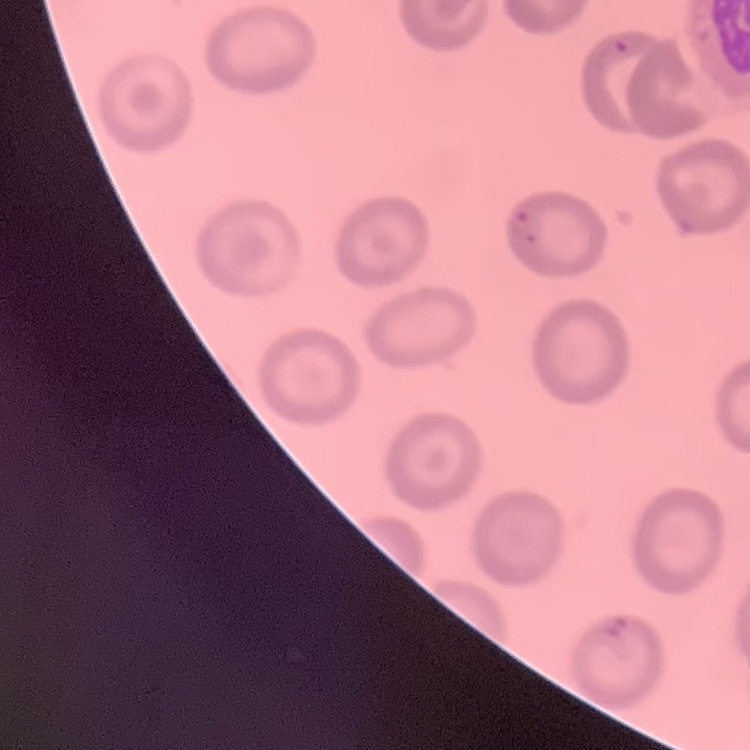
The red blood cells exhibit no rouleaux formation. Stained with either Field's or Giemsa. Thin blood film. Square crop of a larger photomicrograph.